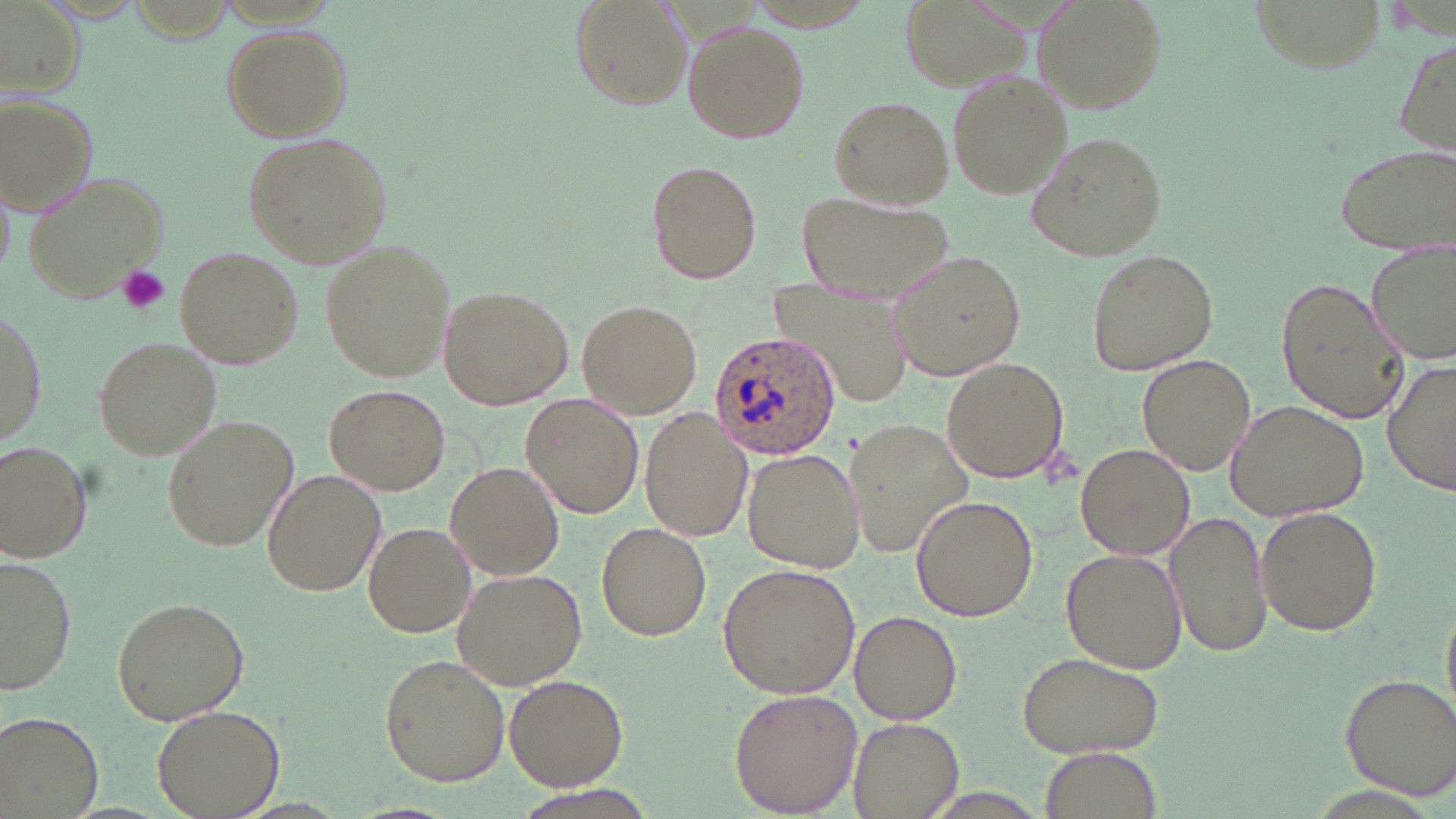 Approximate bounding boxes as [x1, y1, x2, y2] in pixels. Platelet locations: [118, 264, 170, 314]. Plasmodium ovale-infected red blood cell locations: [707, 331, 844, 462]. Uninfected red blood cell locations: [571, 0, 689, 110], [1032, 0, 1168, 113], [1249, 0, 1386, 72], [2, 4, 83, 100], [685, 22, 809, 143], [221, 26, 352, 141], [1395, 38, 1455, 160], [947, 71, 1069, 200], [3, 94, 99, 217], [828, 96, 953, 209], [240, 131, 393, 267], [1026, 131, 1169, 259], [1334, 141, 1456, 255], [646, 160, 762, 285], [21, 169, 171, 305], [798, 192, 957, 305], [1365, 238, 1456, 365], [321, 242, 454, 381], [176, 247, 303, 368], [1085, 248, 1219, 376], [890, 250, 1029, 379], [1276, 274, 1409, 425], [793, 278, 913, 406], [438, 285, 571, 410], [576, 299, 703, 419], [0, 307, 44, 455], [91, 335, 222, 462], [1137, 354, 1255, 475], [1384, 355, 1456, 499], [941, 356, 1070, 484], [325, 384, 450, 495], [522, 394, 644, 518], [1228, 398, 1370, 520], [641, 409, 752, 543], [161, 415, 297, 552], [846, 419, 972, 556], [0, 441, 93, 562], [1077, 443, 1195, 561], [743, 450, 864, 572], [446, 462, 564, 580], [263, 470, 384, 595], [910, 494, 1038, 621], [1256, 504, 1383, 636], [1168, 508, 1268, 661], [597, 521, 711, 642], [364, 522, 476, 638], [1061, 548, 1186, 674], [1, 557, 76, 696], [718, 562, 860, 699], [452, 567, 589, 691], [1441, 590, 1456, 719], [111, 597, 249, 724], [850, 610, 963, 724], [1015, 650, 1168, 758], [378, 654, 511, 787], [1339, 672, 1456, 799], [503, 674, 628, 790], [728, 687, 861, 816], [153, 704, 284, 819], [2, 713, 100, 819], [847, 719, 961, 817], [1042, 749, 1162, 819]. Slide-level diagnosis: Plasmodium ovale. Single field of view. Thin blood film. May-Grünwald-Giemsa-stained preparation. Captured at 1000x magnification. Light microscopy. Image is 1456×819 pixels.